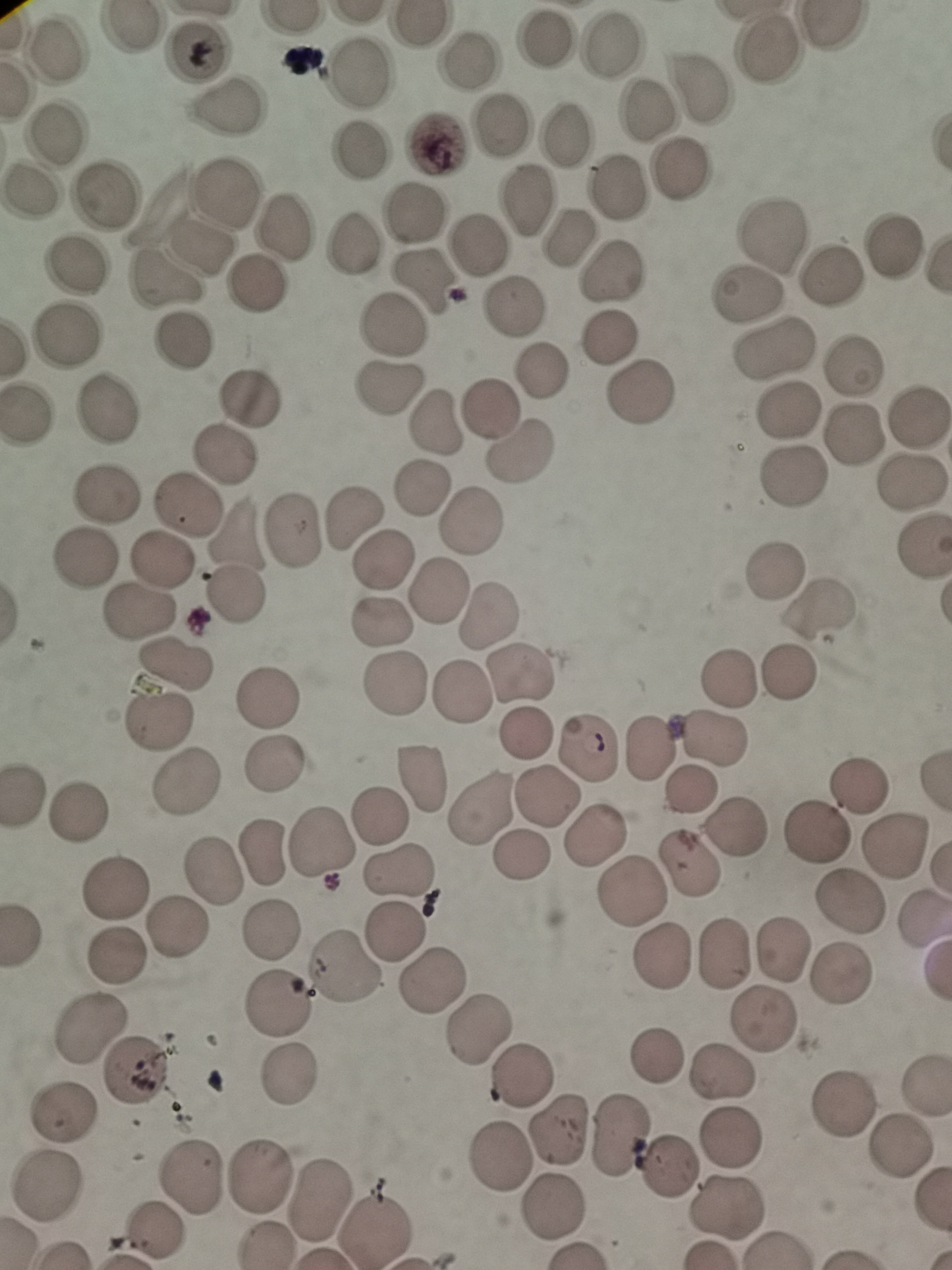
{
  "cell_locations": "approximate centers as [x, y] in pixels: [548, 43], [614, 48], [55, 50], [765, 51], [199, 52], [469, 59], [356, 69], [695, 92], [224, 105], [643, 112], [500, 129], [52, 134], [564, 136], [435, 146], [359, 150], [678, 174], [616, 190], [108, 192], [223, 192], [30, 195], [527, 202], [416, 217], [283, 225], [567, 237], [772, 237], [358, 245], [197, 246], [476, 248], [889, 248], [77, 265], [611, 272], [829, 278], [166, 285], [255, 285], [426, 285], [747, 296], [514, 307], [389, 327], [66, 336], [612, 338], [185, 340], [774, 350], [852, 364], [539, 372], [393, 386], [638, 393], [247, 398], [108, 407], [492, 410], [788, 410], [917, 420], [433, 428], [852, 434], [521, 453], [217, 458], [790, 477], [910, 484], [423, 491], [107, 493], [186, 507], [473, 515], [352, 516], [235, 530], [296, 532], [85, 559], [160, 561], [385, 565], [773, 573], [438, 591], [236, 593], [141, 610], [820, 612], [486, 615], [386, 625], [171, 665], [787, 671], [520, 674], [730, 680], [396, 684], [458, 696], [269, 698], [161, 721], [527, 731], [714, 737], [585, 744], [650, 746], [274, 761], [424, 778], [186, 782], [859, 787], [691, 790], [544, 799], [480, 805], [78, 812], [380, 814], [738, 827], [596, 829], [815, 832], [900, 842], [324, 844], [262, 853], [694, 865], [399, 868], [213, 869], [117, 890], [630, 893], [846, 903], [178, 925], [272, 928], [392, 930], [785, 946], [720, 956], [662, 957], [343, 971], [840, 971], [426, 981], [277, 1000], [759, 1020], [476, 1027], [89, 1028], [658, 1056], [130, 1070], [288, 1072], [523, 1076], [720, 1078], [840, 1101], [65, 1111], [557, 1128], [620, 1132], [732, 1136], [901, 1148], [502, 1159], [671, 1167], [189, 1179], [259, 1181], [45, 1190], [317, 1199], [728, 1207], [552, 1210], [374, 1225]",
  "field_of_view": "single",
  "stain": "Giemsa",
  "preparation": "thin blood smear",
  "capture": "smartphone through the microscope eyepiece",
  "image_size": "952×1270 pixels"
}